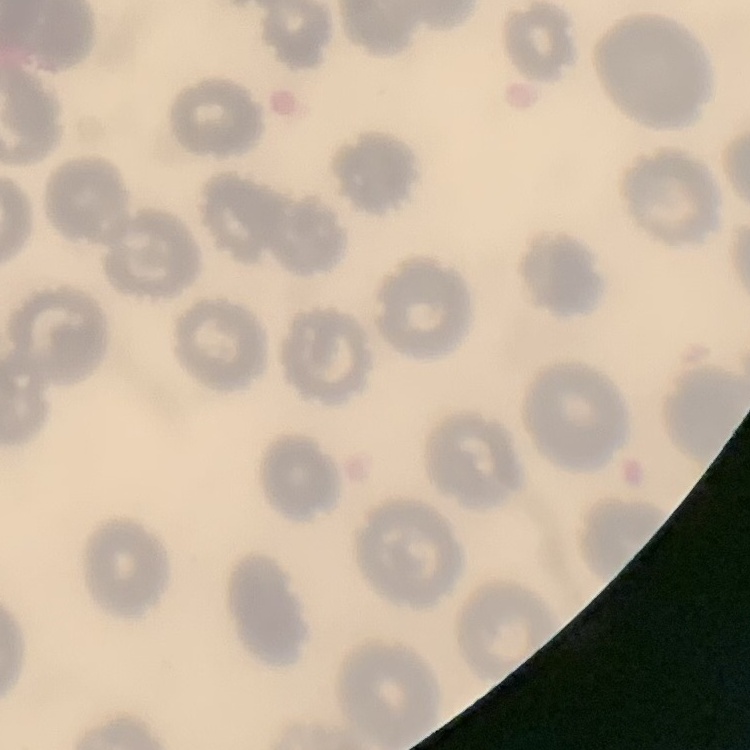
{
  "red_blood_cell_morphology": "no rouleaux formation",
  "image_type": "square crop of a larger photomicrograph",
  "stain": "Field's or Giemsa",
  "preparation": "thin blood smear"
}